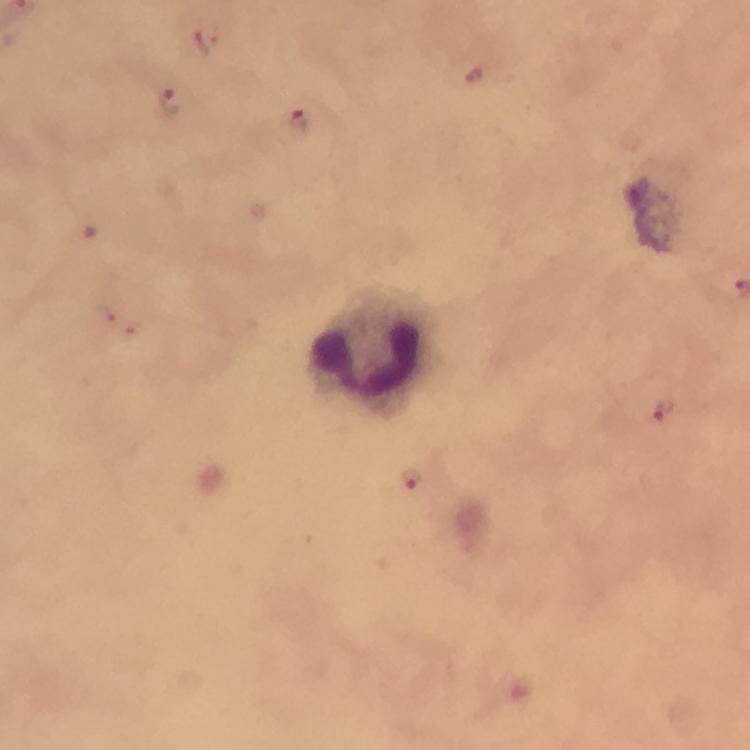
Approximate centers as {x, y} in pixels.
Summary:
  - Plasmodium parasite locations: {207, 36}, {173, 101}, {296, 121}, {661, 408}, {413, 478}
  - Leukocyte locations: {377, 351}
  - Preparation: thick blood film
  - Stain: Giemsa
  - Image size: 750×750 pixels
  - Cropped from: a single field of view
  - Magnification: 100x
  - Capture: smartphone camera through the microscope
  - Immersion oil: applied
  - Context: from a diagnostic examination for malaria